Describe the morphology of the erythrocytes.
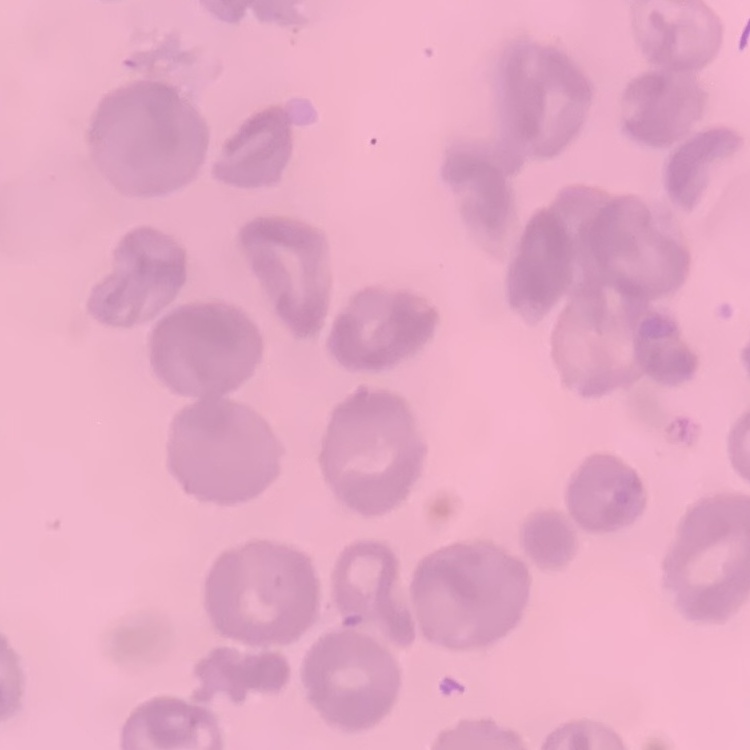

No rouleaux formation.

{
  "image_type": "square crop of a larger photomicrograph",
  "stain": "Field's or Giemsa",
  "preparation": "thin blood film"
}